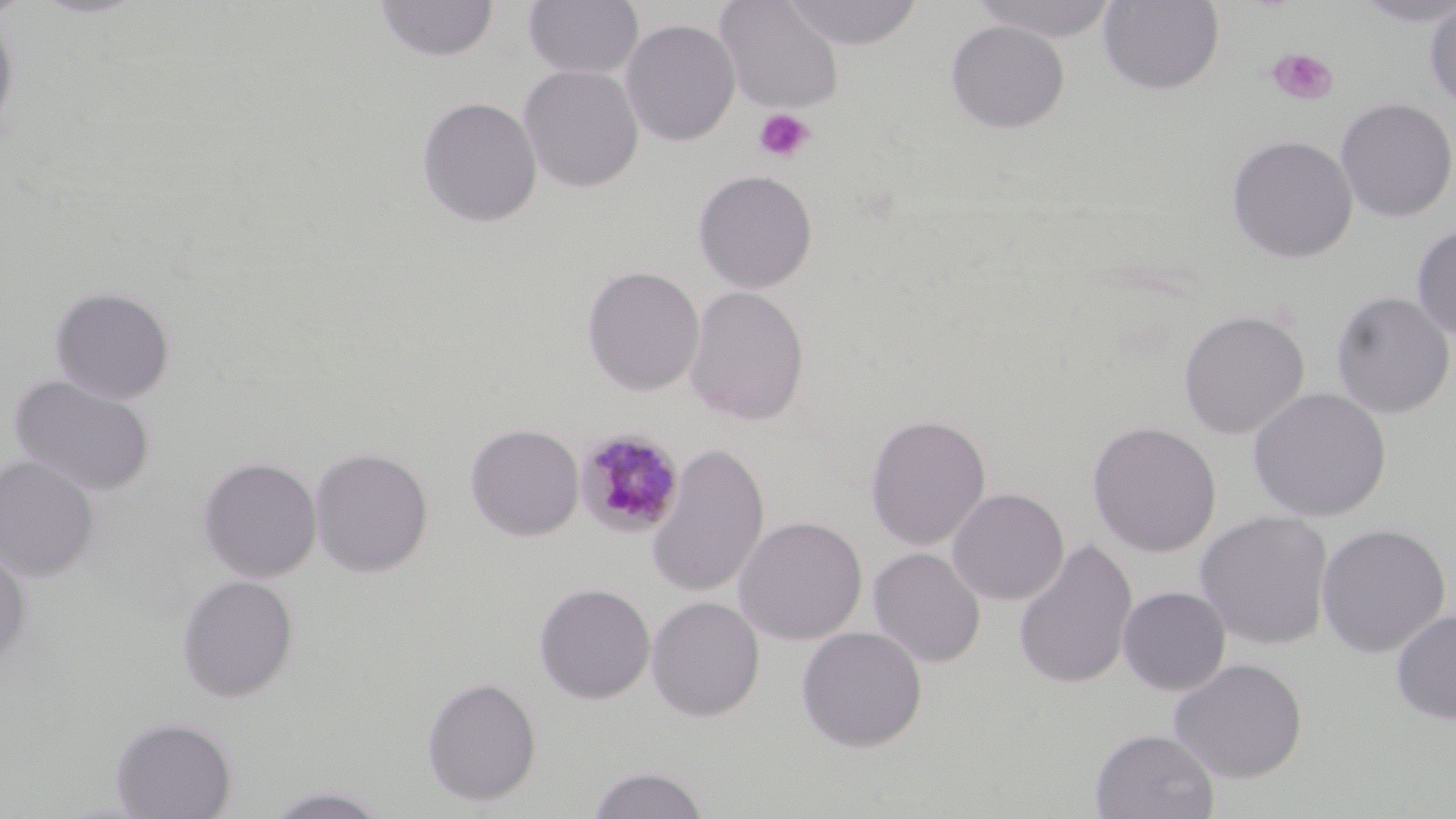

slide-level diagnosis = Plasmodium malariae
magnification = 1000x
stain = May-Grünwald-Giemsa
uninfected red blood cell locations = approximate bounding boxes as named x1/y1/x2/y2 corners in pixels: (x1=29, y1=0, x2=151, y2=19), (x1=375, y1=0, x2=499, y2=62), (x1=523, y1=0, x2=644, y2=80), (x1=714, y1=0, x2=844, y2=114), (x1=783, y1=0, x2=923, y2=49), (x1=969, y1=0, x2=1122, y2=42), (x1=1098, y1=0, x2=1225, y2=95), (x1=1349, y1=0, x2=1456, y2=27), (x1=1423, y1=2, x2=1456, y2=112), (x1=0, y1=10, x2=19, y2=142), (x1=620, y1=19, x2=740, y2=146), (x1=945, y1=20, x2=1070, y2=134), (x1=518, y1=64, x2=644, y2=193), (x1=417, y1=96, x2=543, y2=227), (x1=1335, y1=98, x2=1456, y2=222), (x1=1226, y1=135, x2=1358, y2=264), (x1=693, y1=170, x2=818, y2=293), (x1=1411, y1=224, x2=1456, y2=342), (x1=582, y1=266, x2=704, y2=397), (x1=50, y1=286, x2=175, y2=404), (x1=683, y1=286, x2=810, y2=426), (x1=1331, y1=291, x2=1455, y2=419), (x1=1178, y1=310, x2=1310, y2=440), (x1=9, y1=374, x2=156, y2=497), (x1=1247, y1=387, x2=1392, y2=522), (x1=865, y1=413, x2=991, y2=550), (x1=1087, y1=421, x2=1222, y2=557), (x1=465, y1=423, x2=584, y2=541), (x1=645, y1=442, x2=769, y2=599), (x1=309, y1=447, x2=433, y2=578), (x1=0, y1=455, x2=100, y2=581), (x1=198, y1=457, x2=321, y2=582), (x1=947, y1=487, x2=1069, y2=605), (x1=1195, y1=510, x2=1334, y2=650), (x1=733, y1=515, x2=868, y2=645), (x1=1315, y1=523, x2=1451, y2=658), (x1=1013, y1=539, x2=1138, y2=690), (x1=0, y1=546, x2=31, y2=667), (x1=868, y1=547, x2=985, y2=668), (x1=176, y1=574, x2=299, y2=703), (x1=534, y1=583, x2=655, y2=704), (x1=1118, y1=586, x2=1231, y2=695), (x1=646, y1=595, x2=765, y2=722), (x1=1390, y1=609, x2=1456, y2=725), (x1=796, y1=626, x2=928, y2=752), (x1=1168, y1=658, x2=1308, y2=783), (x1=421, y1=676, x2=542, y2=806), (x1=110, y1=716, x2=237, y2=819), (x1=1090, y1=728, x2=1220, y2=818), (x1=586, y1=766, x2=712, y2=819), (x1=259, y1=786, x2=394, y2=818)
preparation = thin blood smear
field of view = single
modality = light microscopy
Plasmodium malariae-infected red blood cell locations = approximate bounding boxes as named x1/y1/x2/y2 corners in pixels: (x1=575, y1=428, x2=686, y2=539)
image size = 1456×819 pixels
platelet locations = approximate bounding boxes as named x1/y1/x2/y2 corners in pixels: (x1=1266, y1=47, x2=1338, y2=106), (x1=752, y1=107, x2=815, y2=164)